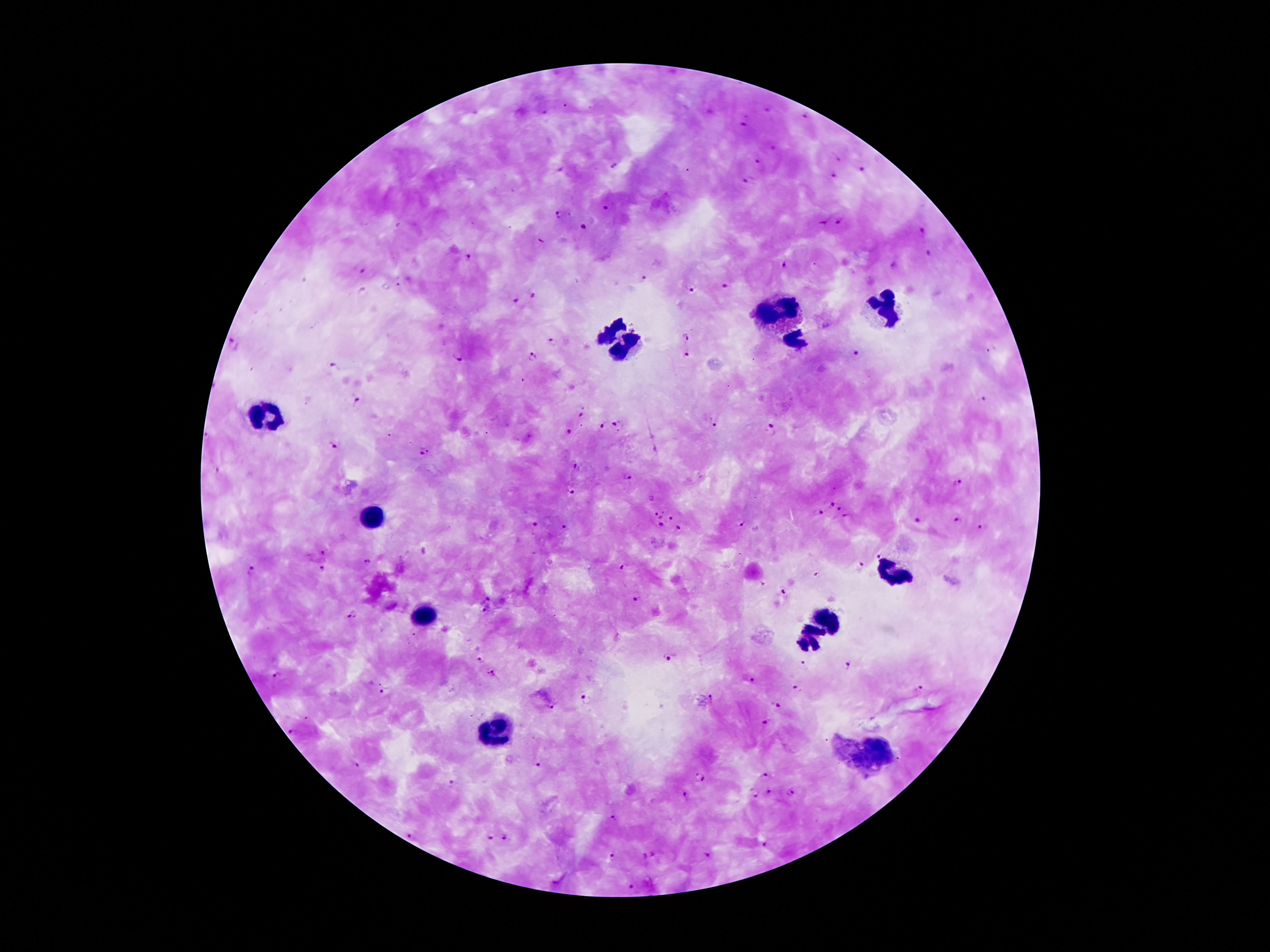
Approximate centers as {x, y} in pixels.
Summary:
  - Plasmodium parasite locations: {565, 107}, {770, 111}, {545, 113}, {807, 117}, {744, 126}, {776, 149}, {839, 158}, {758, 160}, {615, 165}, {561, 170}, {864, 171}, {836, 178}, {746, 182}, {606, 210}, {558, 214}, {839, 221}, {823, 223}, {584, 228}, {921, 231}, {929, 252}, {470, 256}, {895, 265}, {783, 266}, {361, 272}, {642, 277}, {397, 286}, {727, 287}, {691, 289}, {534, 294}, {517, 300}, {686, 337}, {554, 342}, {233, 343}, {856, 354}, {687, 355}, {459, 357}, {531, 358}, {334, 365}, {356, 400}, {984, 400}, {581, 414}, {712, 424}, {600, 426}, {616, 426}, {770, 429}, {569, 431}, {334, 443}, {425, 451}, {575, 466}, {218, 470}, {628, 477}, {956, 483}, {571, 493}, {829, 502}, {840, 507}, {662, 512}, {819, 513}, {656, 514}, {661, 516}, {672, 517}, {847, 517}, {919, 520}, {740, 521}, {959, 521}, {535, 524}, {661, 524}, {565, 527}, {986, 528}, {680, 529}, {321, 550}, {878, 553}, {366, 562}, {859, 564}, {321, 568}, {623, 568}, {252, 570}, {763, 585}, {784, 590}, {489, 598}, {638, 598}, {484, 611}, {354, 615}, {667, 658}, {477, 659}, {803, 664}, {847, 664}, {490, 673}, {279, 674}, {750, 680}, {920, 688}, {385, 689}, {798, 690}, {584, 701}, {778, 704}, {550, 706}, {767, 722}, {293, 733}, {537, 764}, {356, 765}, {699, 776}, {765, 776}, {450, 784}, {770, 791}, {791, 791}, {755, 792}, {684, 795}, {614, 820}, {409, 836}, {492, 836}, {506, 837}, {763, 845}, {655, 854}, {612, 856}, {643, 856}, {707, 856}, {631, 885}
  - Leukocyte locations: {781, 308}, {880, 310}, {611, 328}, {796, 339}, {629, 348}, {273, 414}, {374, 519}, {894, 574}, {423, 617}, {825, 619}, {808, 640}, {497, 728}, {872, 757}
  - Capture: smartphone through the microscope eyepiece
  - Patient malaria status: positive for Plasmodium falciparum
  - Magnification: 100x
  - Image size: 1270×952 pixels
  - Stain: Giemsa
  - Field of view: one from this slide
  - Preparation: thick blood film